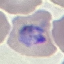
malaria status = parasitized
image type = cell patch, automatically extracted from a larger field of view and resized to 64 × 64 pixels
capture = smartphone camera at the microscope eyepiece
stain = Giemsa
preparation = thin blood smear